Describe the morphology of the erythrocytes.
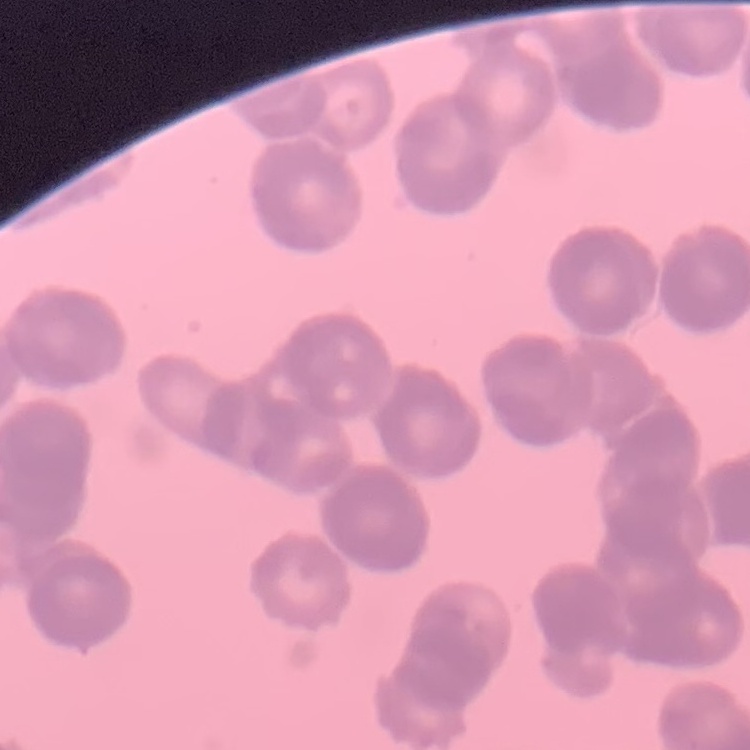

They show rouleaux formation.

Summary:
  - Stain: Field's or Giemsa
  - Preparation: thin blood smear
  - Image type: one tile cut from a larger photomicrograph